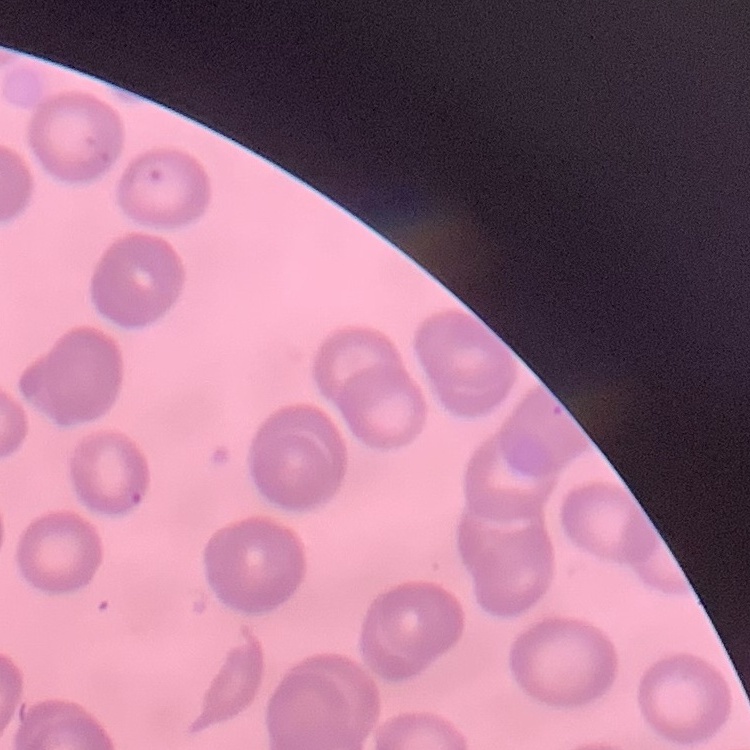
Summary:
  - Erythrocyte morphology: no rouleaux formation
  - Preparation: thin blood film
  - Image type: square crop of a larger photomicrograph
  - Stain: Field's or Giemsa